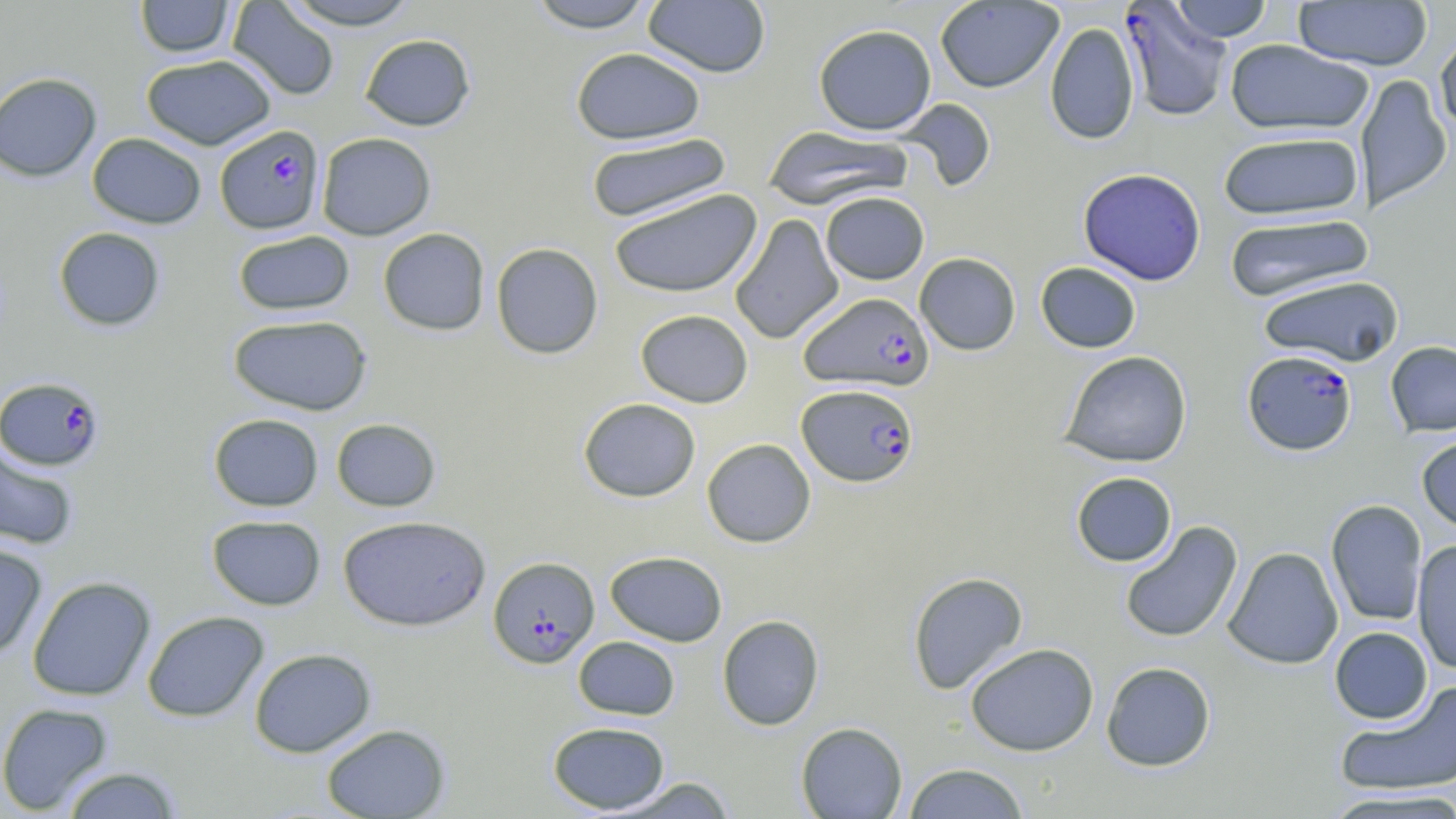
Summary:
  - Coordinate format: approximate bounding boxes as [x1, y1, x2, y2] in pixels
  - Plasmodium falciparum-infected red blood cell locations: [1118, 2, 1231, 122], [214, 124, 326, 235], [799, 291, 934, 392], [1242, 350, 1357, 456], [1, 376, 105, 471], [797, 384, 919, 487], [487, 556, 600, 668]
  - Uninfected red blood cell locations: [135, 0, 235, 59], [278, 0, 424, 30], [526, 0, 656, 32], [643, 0, 771, 77], [226, 1, 340, 101], [934, 1, 1064, 93], [1169, 1, 1274, 42], [1293, 1, 1433, 71], [1044, 22, 1140, 145], [813, 24, 937, 135], [1435, 30, 1456, 141], [360, 33, 476, 130], [1224, 39, 1374, 136], [570, 47, 706, 145], [141, 54, 277, 150], [0, 72, 102, 182], [1356, 73, 1452, 214], [897, 98, 996, 192], [764, 125, 914, 210], [1218, 131, 1365, 221], [87, 132, 207, 229], [316, 132, 436, 240], [586, 132, 732, 224], [1078, 168, 1206, 286], [608, 189, 762, 298], [820, 191, 929, 285], [730, 213, 844, 345], [1223, 213, 1375, 302], [53, 226, 166, 331], [378, 227, 490, 336], [232, 230, 355, 316], [491, 242, 604, 359], [914, 252, 1021, 355], [1035, 261, 1141, 353], [1257, 275, 1404, 367], [635, 309, 754, 408], [228, 314, 373, 415], [1385, 341, 1456, 437], [1059, 350, 1193, 468], [578, 397, 701, 502], [208, 413, 324, 511], [331, 418, 441, 512], [1416, 434, 1456, 536], [702, 438, 816, 547], [0, 445, 80, 550], [1071, 471, 1177, 567], [1326, 499, 1428, 626], [206, 514, 326, 610], [337, 515, 491, 632], [1119, 520, 1243, 644], [1412, 539, 1456, 675], [0, 542, 48, 658], [1223, 546, 1344, 669], [605, 551, 727, 646], [907, 571, 1028, 695], [27, 576, 156, 702], [142, 611, 269, 722], [717, 614, 825, 730], [1329, 627, 1433, 724], [573, 636, 679, 720], [965, 642, 1099, 756], [249, 647, 376, 757], [1101, 661, 1216, 771], [1334, 681, 1456, 797], [0, 702, 115, 816], [547, 721, 670, 814], [795, 722, 908, 818], [321, 723, 450, 818], [902, 762, 1030, 818], [59, 765, 185, 818], [610, 777, 739, 817], [1324, 789, 1456, 818]
  - Slide-level diagnosis: Plasmodium falciparum
  - Magnification: 1000x
  - Stain: May-Grünwald-Giemsa
  - Modality: optical microscopy
  - Image size: 1456×819 pixels
  - Field of view: one of a larger specimen
  - Preparation: thin blood smear